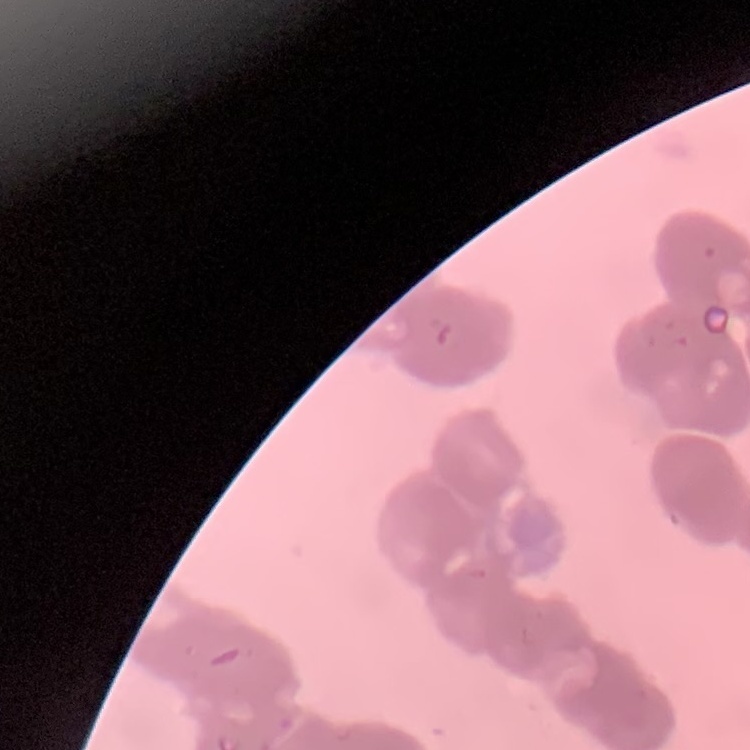

The erythrocytes show rouleaux formation. Field's or Giemsa stain. Square crop of a larger photomicrograph. Thin blood film.